Report the malaria status of this cell.
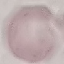
Uninfected.

Summary:
  - Preparation: thin smear
  - Image type: cell patch, automatically extracted from a larger field of view and resized to 64 × 64 pixels
  - Capture: smartphone camera at the microscope eyepiece
  - Stain: Giemsa